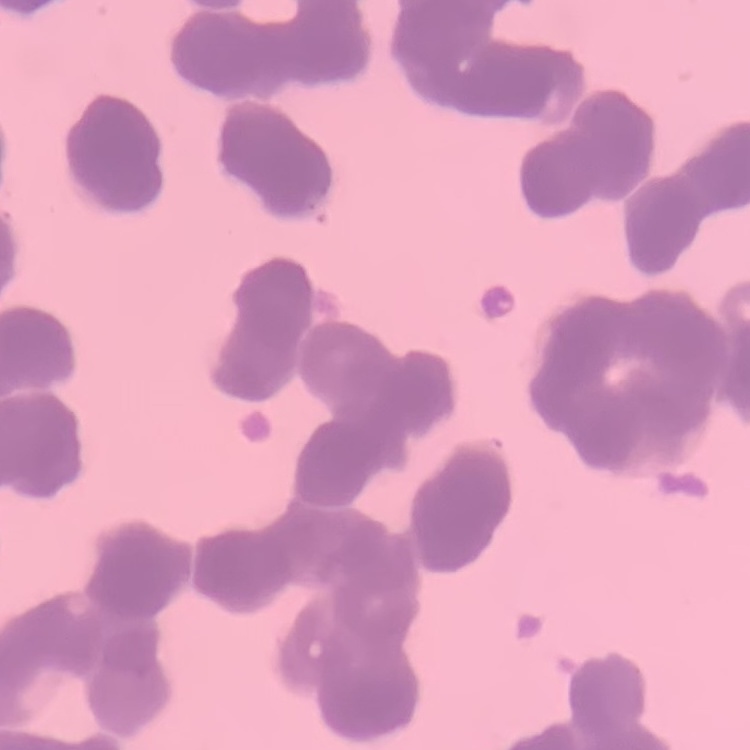
The red blood cells exhibit rouleaux formation. Stained with either Field's or Giemsa. One tile cut from a larger photomicrograph. Thin blood film.